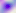 Micrograph. Toxoplasma gondii is seen. 400x magnification.